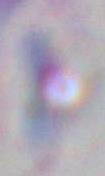 Toxoplasma gondii is shown. Photomicrograph. Captured at 1000x magnification.